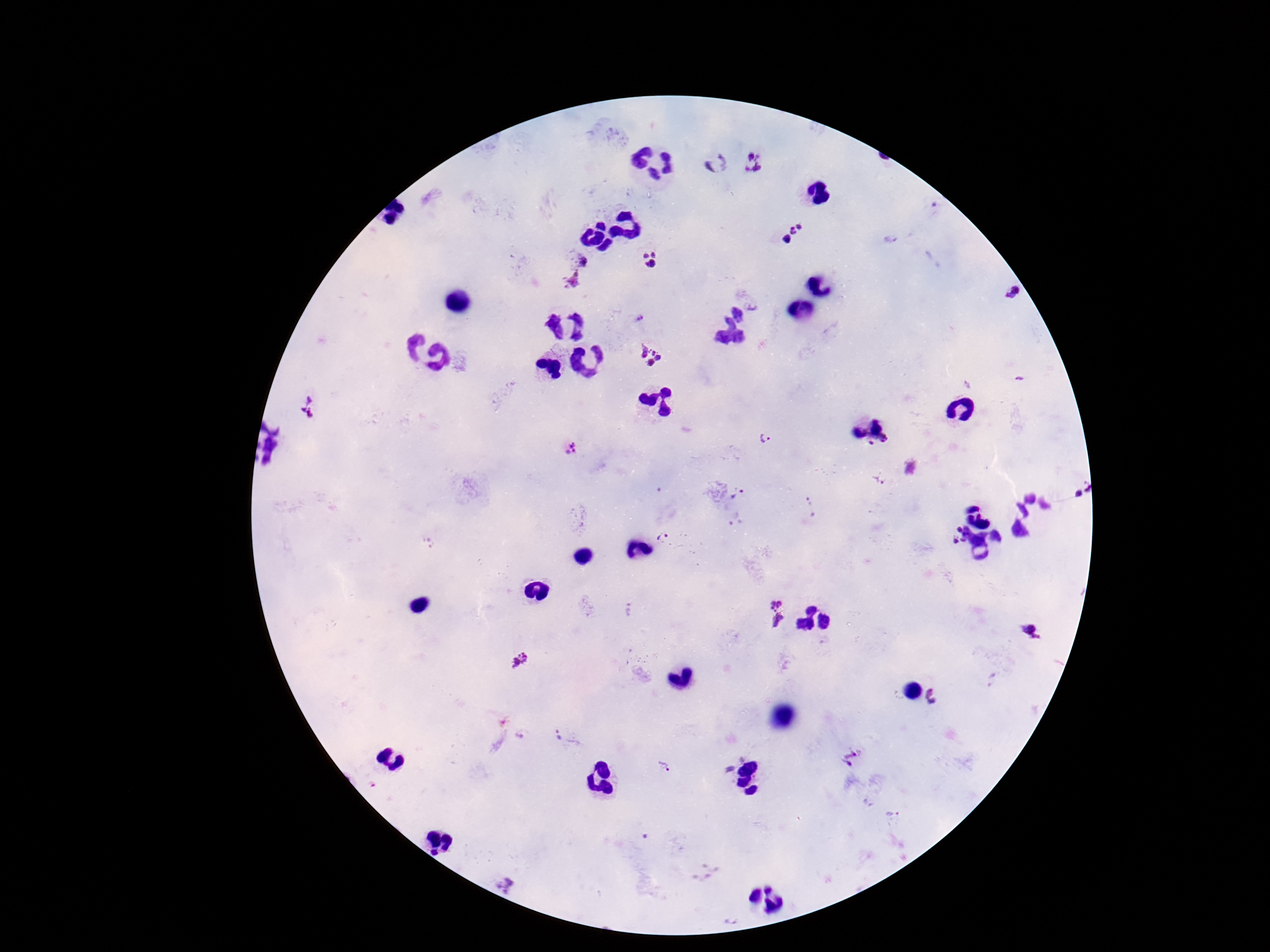

{
  "plasmodium_parasite_locations": "approximate centers as {x, y} in pixels: {715, 164}, {753, 164}, {793, 233}, {652, 260}, {577, 261}, {572, 281}, {1013, 292}, {651, 353}, {308, 405}, {766, 437}, {884, 439}, {872, 444}, {570, 447}, {879, 480}, {1081, 491}, {737, 493}, {959, 529}, {664, 537}, {963, 540}, {956, 541}, {629, 611}, {776, 613}, {1032, 633}, {522, 658}, {935, 696}, {522, 735}, {560, 736}, {851, 758}, {664, 767}, {893, 814}",
  "image_size": "1270×952 pixels",
  "patient_malaria_status": "infected",
  "preparation": "thick peripheral-blood smear",
  "field_of_view": "single",
  "magnification": "100x",
  "capture": "smartphone camera through the microscope eyepiece",
  "stain": "Giemsa"
}